Give the extent of all Plasmodium ovale-infected red blood cells.
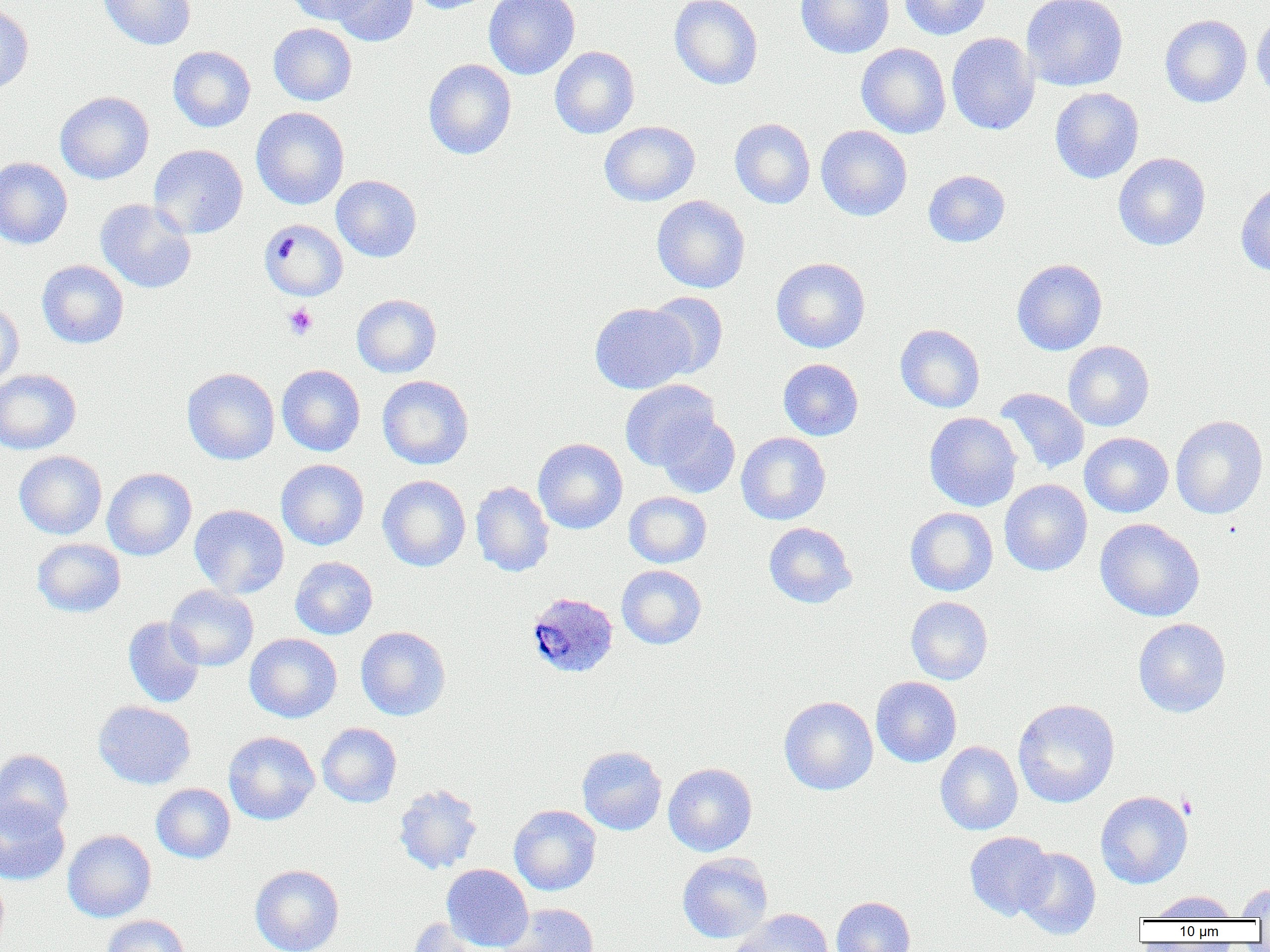

Approximate bounding boxes as (x1, y1, x2, y2) in pixels.
Plasmodium ovale-infected red blood cells: (525, 591, 619, 678).

Uninfected red blood cell locations: (97, 0, 197, 50), (286, 0, 378, 24), (328, 0, 420, 46), (409, 0, 495, 14), (484, 0, 580, 79), (669, 0, 763, 90), (795, 0, 895, 59), (899, 0, 990, 40), (1022, 0, 1128, 91), (0, 3, 34, 95), (1251, 11, 1270, 100), (1160, 14, 1252, 107), (268, 23, 357, 105), (946, 32, 1040, 135), (856, 43, 951, 138), (167, 46, 256, 132), (550, 46, 639, 138), (423, 59, 517, 159), (1050, 88, 1144, 184), (55, 91, 154, 184), (251, 107, 349, 209), (729, 118, 816, 209), (599, 121, 700, 206), (816, 125, 912, 220), (149, 144, 248, 239), (1113, 152, 1210, 251), (0, 157, 72, 249), (923, 170, 1010, 247), (331, 175, 422, 262), (1236, 179, 1270, 277), (651, 195, 750, 293), (95, 199, 197, 293), (259, 219, 348, 301), (771, 257, 871, 353), (1012, 258, 1107, 355), (36, 260, 129, 348), (645, 291, 728, 378), (351, 294, 441, 378), (0, 300, 24, 385), (590, 302, 694, 394), (895, 324, 985, 412), (1063, 340, 1154, 431), (778, 358, 863, 440), (277, 364, 365, 456), (182, 367, 280, 465), (0, 369, 81, 454), (377, 375, 473, 469), (620, 379, 719, 470), (995, 387, 1089, 473), (924, 412, 1022, 511), (655, 413, 740, 498), (1170, 415, 1268, 519), (736, 432, 831, 525), (1079, 432, 1173, 517), (533, 438, 628, 533), (14, 451, 107, 539), (276, 459, 369, 550), (102, 468, 197, 560), (378, 475, 471, 571), (999, 479, 1092, 576), (470, 480, 554, 577), (624, 491, 711, 568), (189, 504, 289, 599), (905, 507, 998, 596), (1095, 518, 1204, 622), (764, 522, 856, 608), (32, 538, 126, 617), (290, 556, 377, 639), (616, 565, 707, 649), (165, 585, 259, 671), (906, 596, 993, 685), (123, 616, 206, 708), (1133, 618, 1231, 717), (355, 626, 451, 720), (245, 633, 342, 722), (871, 676, 961, 767), (779, 696, 878, 795), (1012, 698, 1120, 808), (93, 700, 196, 789), (317, 723, 402, 807), (223, 731, 320, 825), (935, 741, 1023, 835), (577, 746, 667, 835), (0, 749, 73, 835), (663, 762, 757, 856), (151, 783, 235, 864), (393, 783, 484, 875), (1095, 791, 1193, 889), (0, 797, 70, 885), (509, 804, 601, 895), (62, 829, 156, 922), (965, 831, 1055, 920), (1014, 847, 1100, 940), (677, 852, 773, 943), (441, 863, 533, 951), (249, 864, 344, 952), (0, 869, 9, 950), (1236, 883, 1270, 919), (1149, 890, 1237, 921), (831, 896, 915, 952), (502, 903, 599, 952), (729, 908, 833, 952), (100, 915, 190, 952), (407, 917, 495, 951). Platelet locations: (284, 303, 318, 340). Slide-level diagnosis: Plasmodium ovale. Image is 1270×952 pixels. One field of a larger specimen. Captured at 1000x magnification. Thin blood film. Light microscopy.